Give the extent of all Plasmodium ovale-infected red blood cells.
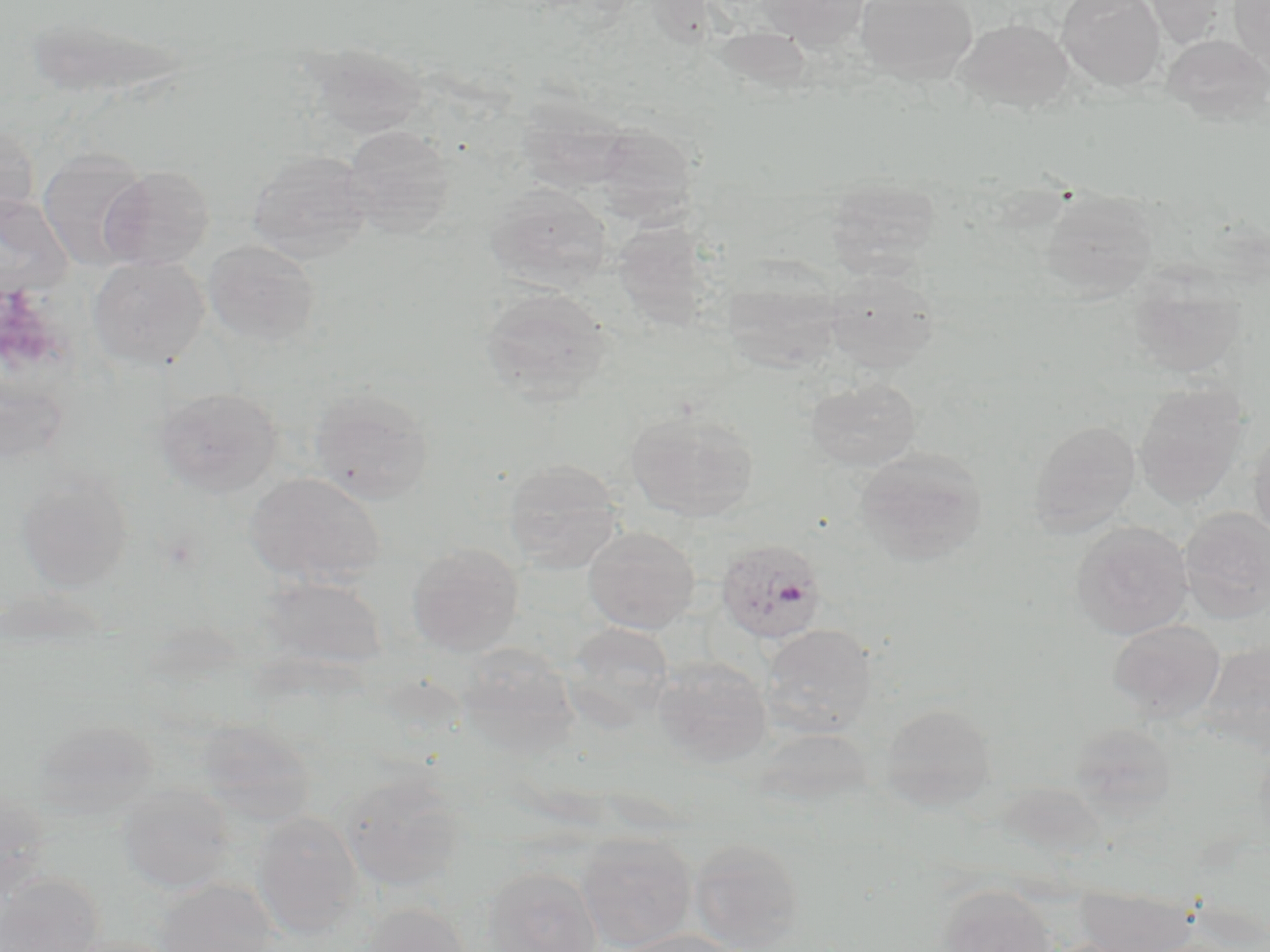

Approximate bounding boxes as (x1, y1, x2, y2) in pixels.
Plasmodium ovale-infected red blood cells: (716, 537, 827, 643).

Summary:
  - Uninfected red blood cell locations: (755, 0, 870, 49), (855, 0, 978, 83), (1057, 0, 1165, 90), (1230, 0, 1270, 78), (1142, 1, 1231, 48), (955, 18, 1075, 114), (30, 20, 192, 98), (1161, 34, 1270, 125), (308, 42, 428, 140), (515, 97, 634, 192), (0, 121, 39, 227), (594, 123, 699, 225), (342, 124, 457, 236), (37, 150, 152, 271), (246, 150, 373, 262), (100, 165, 215, 269), (824, 178, 940, 275), (486, 183, 613, 291), (1039, 189, 1159, 302), (1, 195, 74, 297), (616, 215, 721, 336), (202, 239, 320, 348), (88, 256, 209, 370), (720, 268, 844, 372), (823, 268, 938, 371), (1126, 271, 1246, 380), (479, 287, 613, 404), (804, 376, 921, 471), (1134, 383, 1249, 509), (309, 386, 435, 504), (156, 387, 282, 497), (626, 408, 759, 522), (1029, 419, 1141, 536), (1249, 423, 1270, 544), (854, 447, 988, 565), (502, 458, 625, 572), (15, 469, 135, 592), (245, 471, 386, 587), (1179, 507, 1270, 623), (1071, 521, 1193, 639), (582, 525, 701, 634), (407, 543, 524, 656), (259, 574, 389, 671), (1108, 619, 1225, 721), (563, 621, 677, 729), (760, 623, 878, 738), (1199, 640, 1270, 755), (454, 642, 582, 762), (652, 656, 773, 769), (880, 703, 996, 810), (29, 717, 158, 821), (194, 718, 316, 824), (1067, 720, 1178, 817), (341, 772, 468, 893), (117, 784, 236, 894), (1, 787, 53, 900), (251, 811, 365, 937), (576, 833, 697, 951), (688, 837, 806, 950), (480, 866, 601, 951), (0, 874, 103, 952), (155, 880, 279, 951), (1074, 883, 1199, 952), (937, 884, 1057, 952), (361, 902, 473, 952), (612, 929, 743, 952), (57, 935, 183, 952)
  - Slide-level diagnosis: Plasmodium ovale
  - Magnification: 1000x
  - Image size: 1270×952 pixels
  - Modality: light microscopy
  - Preparation: thin blood smear
  - Field of view: one of a larger specimen
  - Stain: May-Grünwald-Giemsa